Identify the parasite.
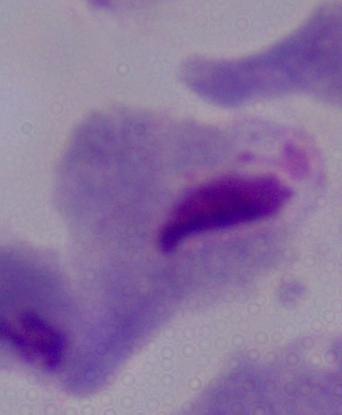

This is a trichomonad.

magnification = 1000x
modality = micrograph